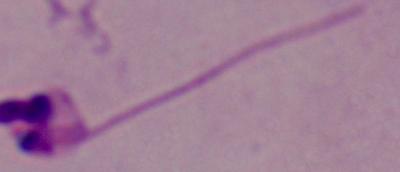
identification = Leishmania
modality = photomicrograph
magnification = 1000x